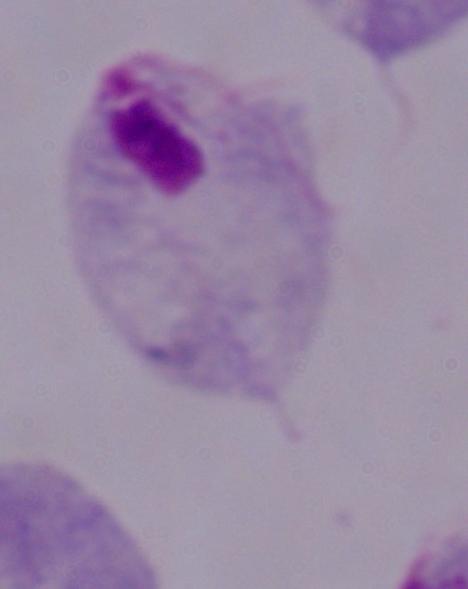
Summary:
  - Magnification: 1000x
  - Modality: micrograph
  - Identification: trichomonad